Comment on the morphology of the red blood cells.
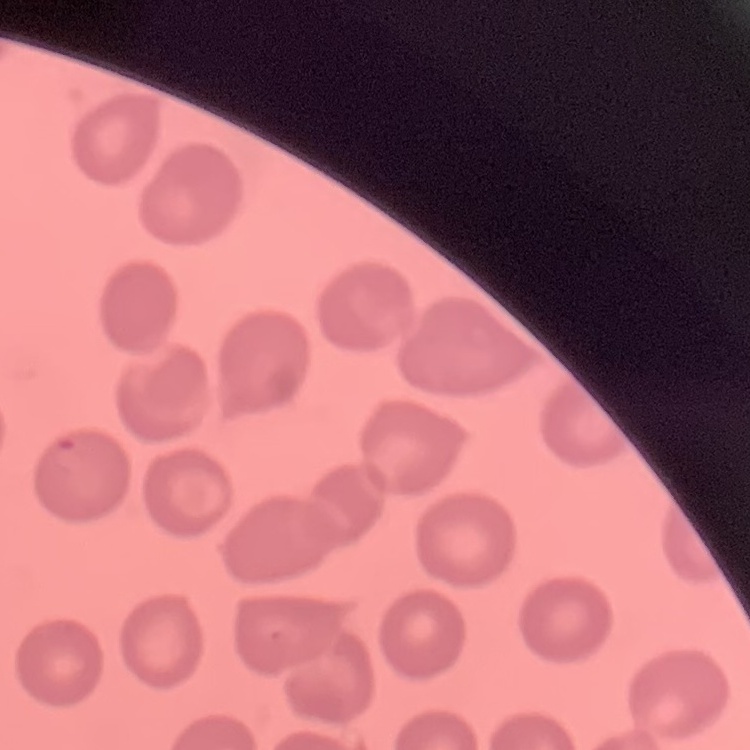

They show no rouleaux formation.

stain = Field's or Giemsa
preparation = thin blood smear
image type = one tile cut from a larger photomicrograph